Comment on the morphology of the red blood cells.
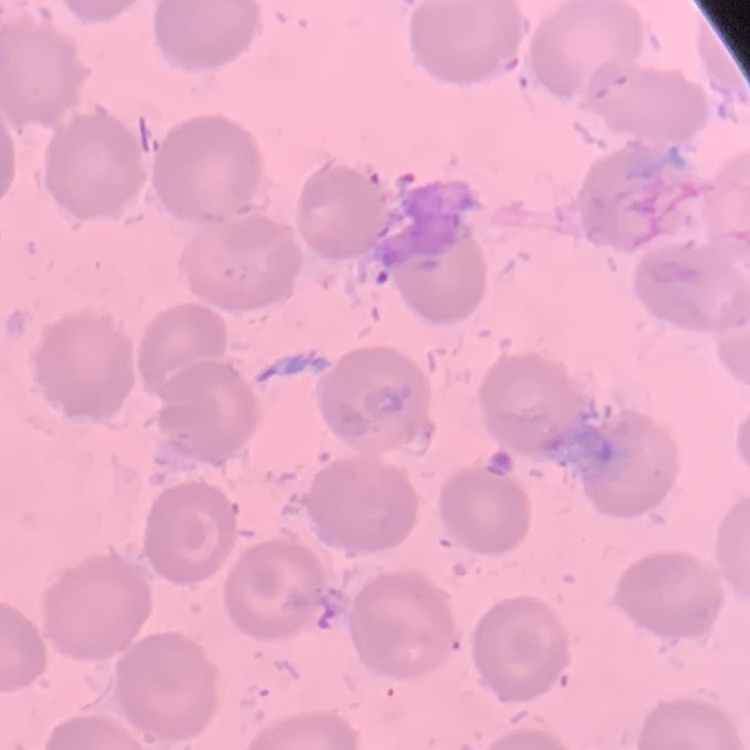
They show no rouleaux formation.

stain = Field's or Giemsa
image type = square crop of a larger photomicrograph
preparation = thin peripheral smear